Locate every uninfected red blood cell.
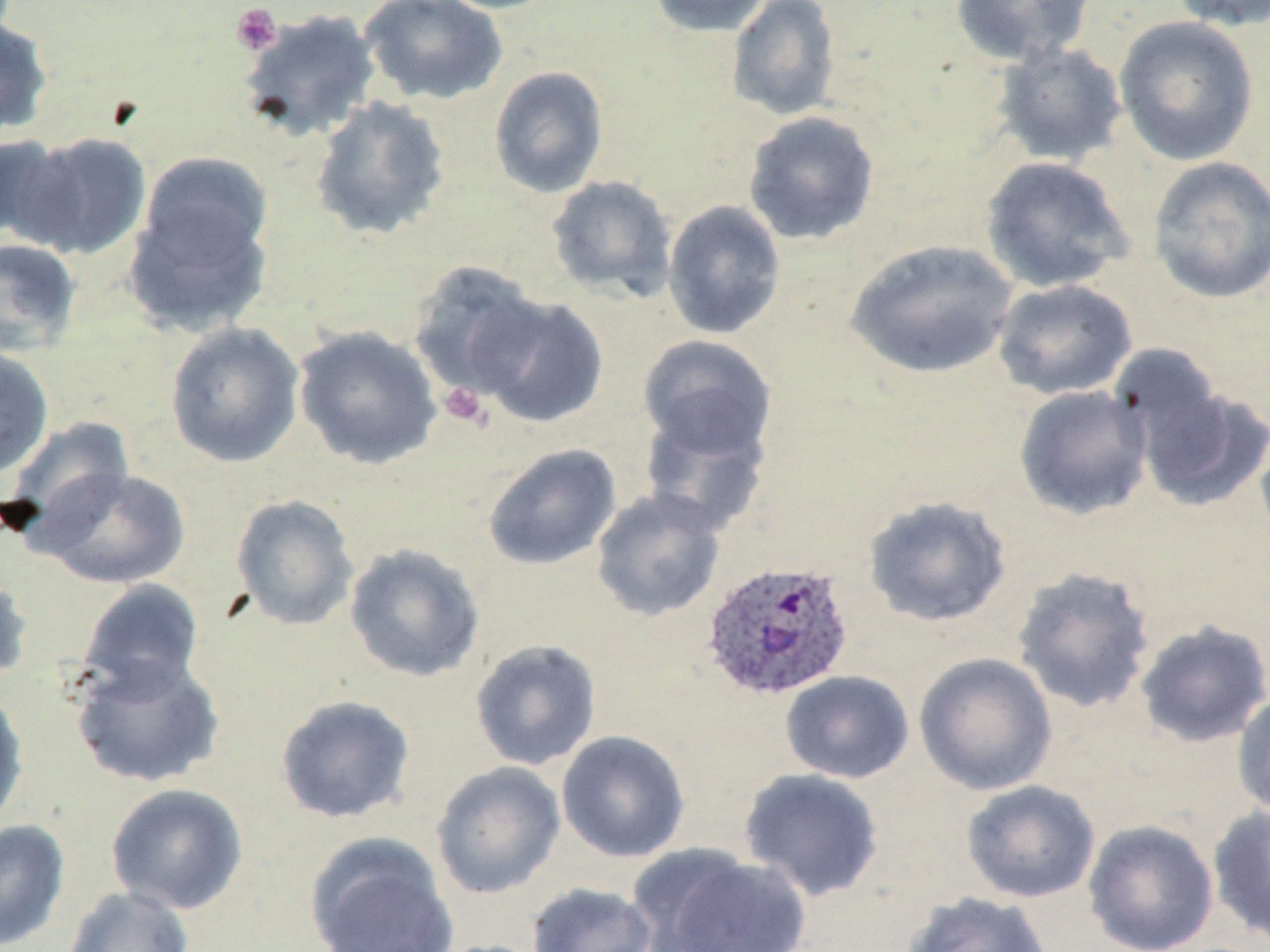

Approximate bounding boxes as (x1,y1)-(x2,y2) corner pairs in pixels.
Uninfected red blood cells: (359,0)-(508,106), (431,0)-(564,14), (646,0)-(773,36), (727,0)-(841,121), (949,0)-(1096,66), (1166,0)-(1270,32), (238,8)-(382,142), (0,13)-(53,141), (1114,16)-(1259,166), (991,41)-(1128,166), (488,65)-(608,198), (310,95)-(451,240), (742,110)-(881,246), (14,131)-(152,260), (0,134)-(73,244), (136,152)-(274,274), (979,155)-(1135,294), (1146,156)-(1270,304), (546,175)-(678,302), (123,186)-(273,337), (662,199)-(786,340), (0,237)-(81,356), (845,239)-(1019,380), (408,261)-(546,399), (992,279)-(1138,401), (475,294)-(609,428), (164,322)-(305,468), (293,326)-(442,470), (637,334)-(778,465), (0,346)-(54,479), (1134,384)-(1270,512), (1014,385)-(1153,521), (639,401)-(772,537), (5,416)-(135,546), (1254,418)-(1270,553), (481,443)-(623,570), (41,468)-(190,589), (591,488)-(726,622), (230,493)-(360,631), (862,495)-(1013,628), (344,543)-(486,683), (1011,566)-(1156,713), (0,568)-(33,689), (78,578)-(204,699), (1134,619)-(1270,747), (470,639)-(602,770), (913,651)-(1058,796), (71,654)-(224,788), (780,670)-(915,783), (0,688)-(29,829), (1232,690)-(1270,820), (275,694)-(416,824), (556,730)-(690,863), (430,761)-(566,898), (738,768)-(886,903), (960,780)-(1101,903), (105,782)-(249,915), (1208,805)-(1270,946), (0,818)-(70,950), (1082,819)-(1219,952), (306,832)-(459,952), (631,846)-(813,952), (526,882)-(658,952), (62,885)-(194,952), (901,891)-(1055,952).

Summary:
  - Platelet locations: (230,3)-(282,56), (437,381)-(489,429)
  - Plasmodium ovale-infected red blood cell locations: (699,559)-(855,701)
  - Slide-level diagnosis: Plasmodium ovale
  - Image size: 1270×952 pixels
  - Preparation: thin blood film
  - Field of view: single
  - Stain: May-Grünwald-Giemsa
  - Magnification: 1000x
  - Modality: optical microscopy